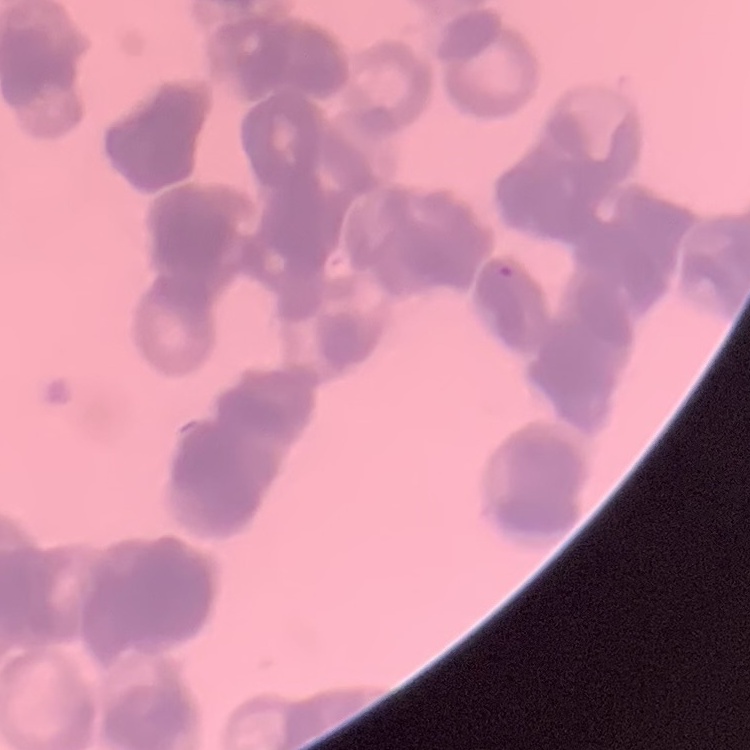 The red blood cells exhibit rouleaux formation. Square crop of a larger photomicrograph. Stained with either Field's or Giemsa. Thin peripheral smear.